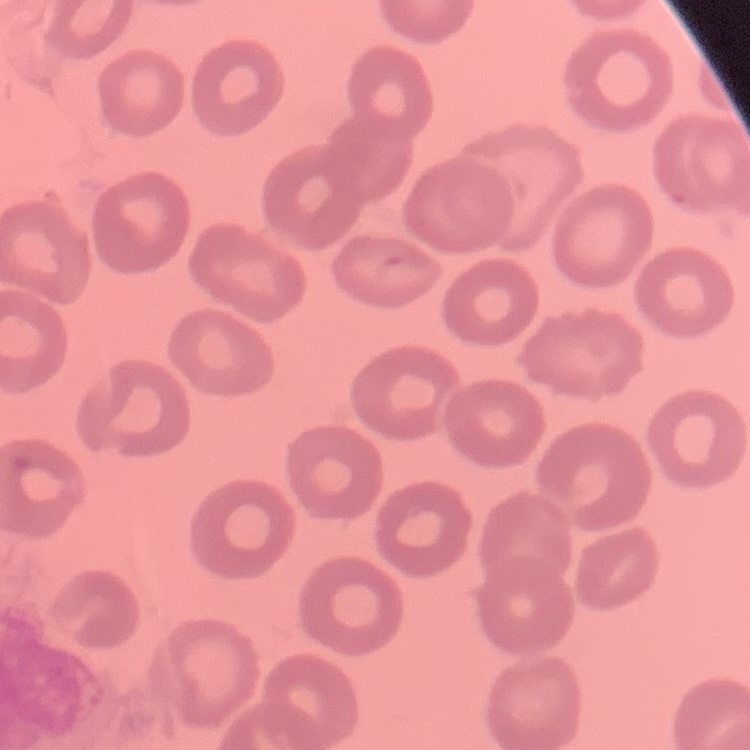

erythrocyte_morphology: no rouleaux formation
stain: Field's or Giemsa
preparation: thin blood smear
image_type: one tile cut from a larger photomicrograph